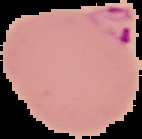

image size = 142×139 pixels
image type = cell region segmented out of the field of view; surrounding area masked to black
malaria status = parasitized
preparation = thin blood smear